State which parasite is depicted.
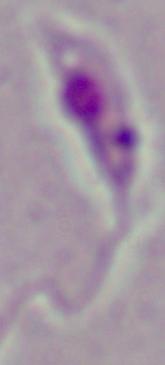
This is Leishmania.

1000x magnification. Photomicrograph.